Report the malaria status of this cell.
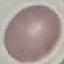
Uninfected.

Photographed with a smartphone camera at the microscope eyepiece. Thin blood film. Automatically extracted cell patch, resized to 64 × 64 pixels. Giemsa-stained preparation.